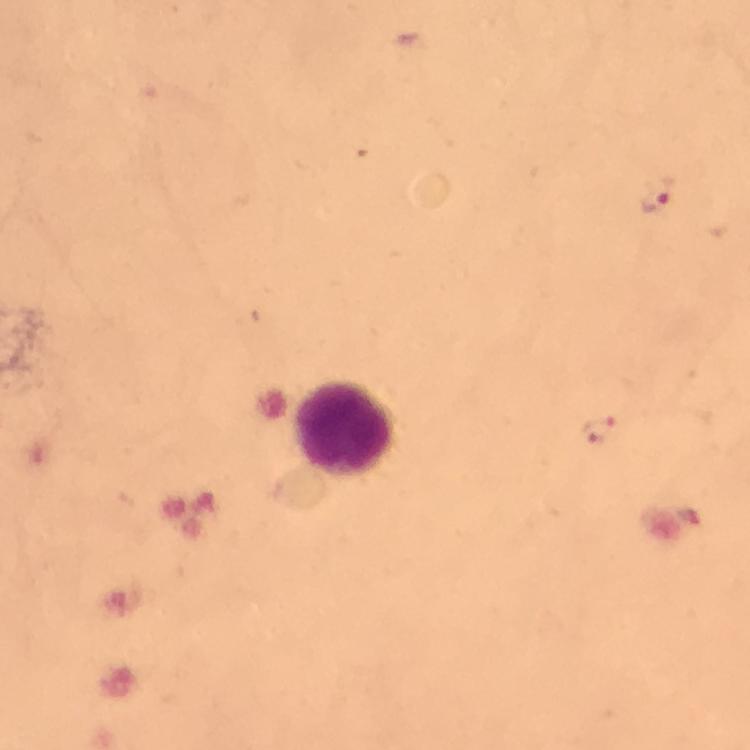

Approximate centers as [x, y] in pixels.
Summary:
  - Leukocyte locations: [346, 430]
  - Malaria parasite locations: [654, 194], [597, 430]
  - Capture: smartphone mounted on the microscope
  - Magnification: 100x
  - Immersion oil: used
  - Stain: Giemsa
  - Image size: 750×750 pixels
  - Preparation: thick blood film
  - Context: from a malaria diagnostic workup
  - Cropped from: one field of view